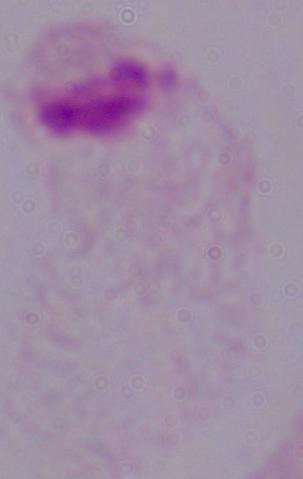

modality = photomicrograph
magnification = 1000x
identification = trichomonad